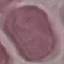 Result: no malaria parasites seen. Cell patch, automatically extracted from a larger field of view and resized to 64 × 64 pixels. Thin blood smear. Giemsa-stained preparation. Photographed with a smartphone camera at the microscope eyepiece.